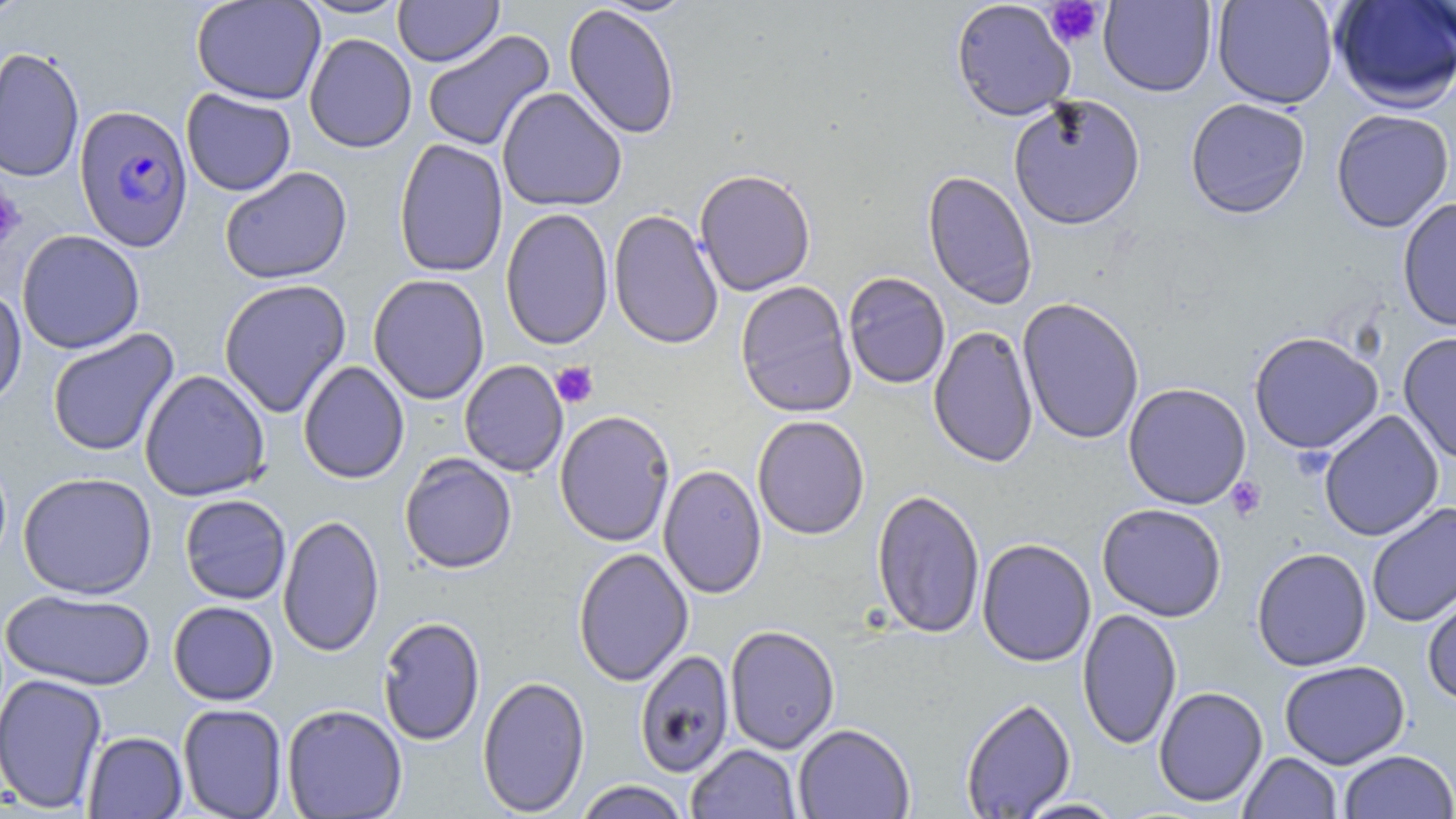

Approximate bounding boxes as named x1/y1/x2/y2 corners in pixels. Plasmodium falciparum-infected red blood cell locations: (x1=73, y1=104, x2=193, y2=253). Uninfected red blood cell locations: (x1=0, y1=0, x2=29, y2=24), (x1=190, y1=0, x2=326, y2=105), (x1=297, y1=0, x2=409, y2=20), (x1=393, y1=0, x2=504, y2=66), (x1=597, y1=0, x2=697, y2=16), (x1=950, y1=0, x2=1076, y2=122), (x1=1099, y1=0, x2=1217, y2=96), (x1=1212, y1=0, x2=1338, y2=109), (x1=1331, y1=0, x2=1456, y2=112), (x1=563, y1=3, x2=680, y2=140), (x1=422, y1=30, x2=555, y2=152), (x1=304, y1=33, x2=417, y2=153), (x1=0, y1=47, x2=84, y2=183), (x1=496, y1=87, x2=627, y2=212), (x1=181, y1=88, x2=297, y2=196), (x1=1008, y1=94, x2=1146, y2=229), (x1=1185, y1=97, x2=1311, y2=219), (x1=1331, y1=109, x2=1455, y2=233), (x1=393, y1=138, x2=509, y2=278), (x1=219, y1=166, x2=353, y2=284), (x1=694, y1=168, x2=816, y2=296), (x1=922, y1=170, x2=1038, y2=309), (x1=1398, y1=197, x2=1456, y2=333), (x1=500, y1=208, x2=614, y2=350), (x1=608, y1=209, x2=723, y2=350), (x1=17, y1=230, x2=145, y2=353), (x1=843, y1=271, x2=950, y2=389), (x1=368, y1=274, x2=490, y2=404), (x1=218, y1=279, x2=352, y2=418), (x1=735, y1=280, x2=857, y2=417), (x1=0, y1=283, x2=27, y2=409), (x1=1017, y1=297, x2=1145, y2=445), (x1=928, y1=325, x2=1039, y2=467), (x1=46, y1=330, x2=180, y2=457), (x1=1248, y1=331, x2=1384, y2=454), (x1=1398, y1=331, x2=1456, y2=464), (x1=459, y1=360, x2=568, y2=477), (x1=298, y1=361, x2=410, y2=484), (x1=139, y1=369, x2=271, y2=501), (x1=1123, y1=382, x2=1252, y2=509), (x1=554, y1=409, x2=675, y2=547), (x1=1319, y1=410, x2=1444, y2=542), (x1=752, y1=414, x2=870, y2=540), (x1=399, y1=453, x2=517, y2=573), (x1=658, y1=464, x2=767, y2=600), (x1=18, y1=472, x2=157, y2=599), (x1=872, y1=488, x2=985, y2=639), (x1=179, y1=494, x2=291, y2=604), (x1=1366, y1=502, x2=1456, y2=628), (x1=1097, y1=503, x2=1227, y2=622), (x1=277, y1=514, x2=385, y2=657), (x1=976, y1=538, x2=1096, y2=666), (x1=572, y1=547, x2=694, y2=686), (x1=1252, y1=547, x2=1372, y2=671), (x1=1422, y1=583, x2=1456, y2=707), (x1=1, y1=589, x2=155, y2=691), (x1=167, y1=601, x2=279, y2=705), (x1=1077, y1=608, x2=1182, y2=750), (x1=378, y1=616, x2=486, y2=746), (x1=724, y1=625, x2=840, y2=754), (x1=635, y1=649, x2=734, y2=777), (x1=1279, y1=660, x2=1410, y2=769), (x1=0, y1=673, x2=108, y2=814), (x1=477, y1=675, x2=590, y2=816), (x1=1153, y1=686, x2=1268, y2=807), (x1=961, y1=697, x2=1076, y2=818), (x1=177, y1=703, x2=288, y2=819), (x1=282, y1=704, x2=408, y2=818), (x1=793, y1=723, x2=915, y2=819), (x1=82, y1=731, x2=188, y2=818), (x1=686, y1=743, x2=802, y2=818), (x1=1339, y1=750, x2=1456, y2=819), (x1=1239, y1=752, x2=1342, y2=819), (x1=574, y1=780, x2=691, y2=819), (x1=1012, y1=797, x2=1128, y2=818). Platelet locations: (x1=1044, y1=1, x2=1104, y2=49), (x1=0, y1=181, x2=25, y2=253), (x1=550, y1=361, x2=599, y2=408), (x1=1225, y1=476, x2=1266, y2=521). Slide-level diagnosis: Plasmodium falciparum. Single field of view. Optical microscopy. 1000x magnification. May-Grünwald-Giemsa-stained preparation. Image is 1456×819 pixels. Thin blood film.